State which parasite is depicted.
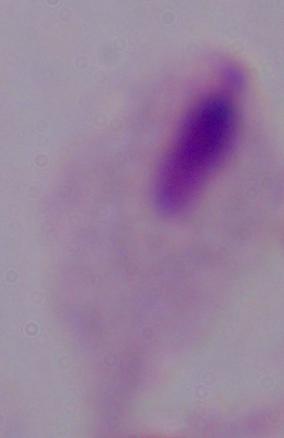

A trichomonad.

Summary:
  - Magnification: 1000x
  - Modality: micrograph